Classify this cell by malaria status.
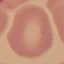
It is uninfected.

preparation = thin blood film
stain = Giemsa
image type = automatically extracted cell patch, resized to 64 × 64 pixels
capture = smartphone camera at the microscope eyepiece